Identify the parasite.
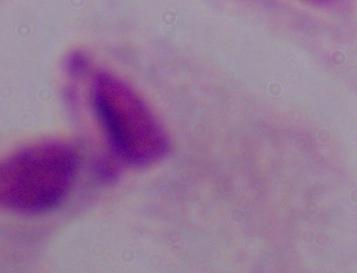

This is a trichomonad.

magnification = 1000x
modality = micrograph